Describe the morphology of the red blood cells.
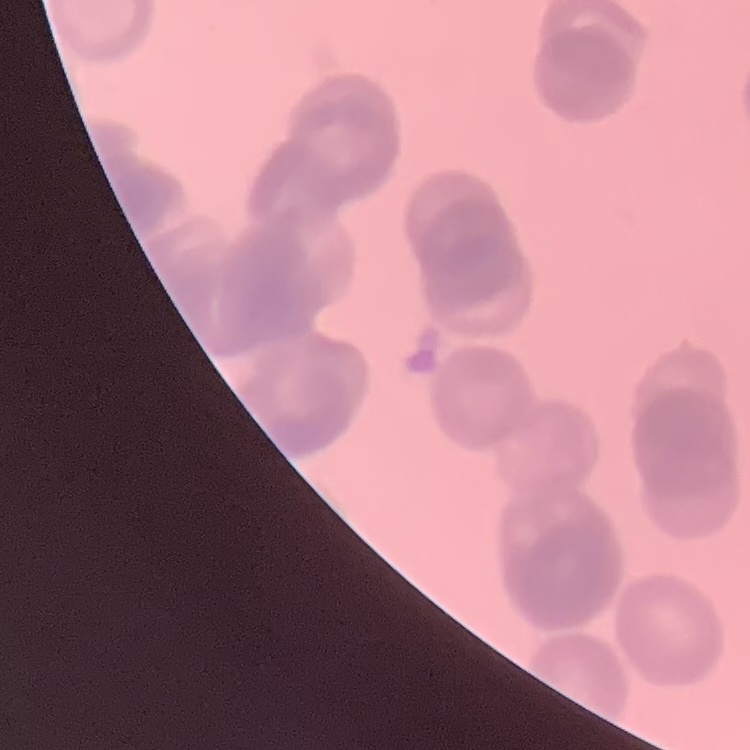

Rouleaux formation.

Thin blood smear. Field's or Giemsa stain. One tile cut from a larger photomicrograph.